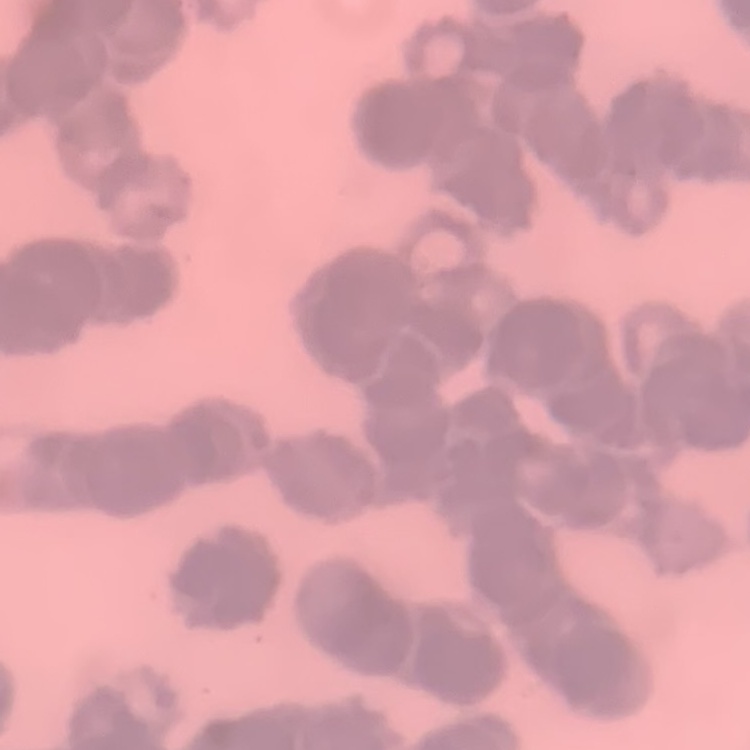

erythrocyte morphology = rouleaux formation
stain = Field's or Giemsa
preparation = thin peripheral smear
image type = one tile cut from a larger photomicrograph